Outline each uninfected red blood cell.
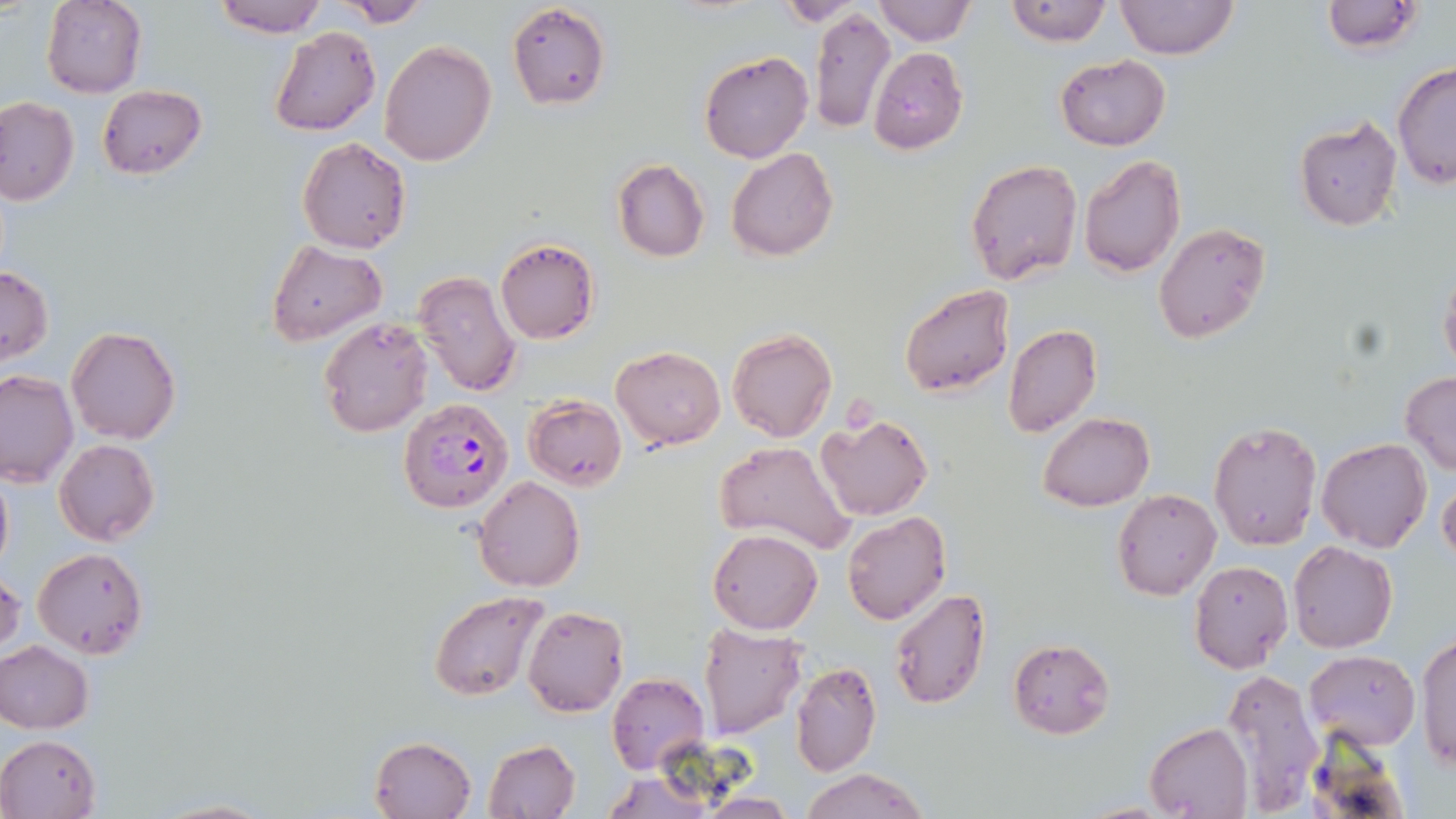

Approximate bounding boxes as (x1,y1)-(x2,y2) corner pairs in pixels.
Uninfected red blood cells: (41,0)-(147,98), (211,0)-(327,38), (337,0)-(432,27), (872,0)-(975,46), (1005,0)-(1111,46), (1113,0)-(1238,61), (776,1)-(862,24), (1321,1)-(1422,53), (506,2)-(611,112), (810,8)-(896,134), (269,27)-(380,136), (378,40)-(497,166), (869,47)-(969,151), (699,50)-(813,163), (1055,55)-(1170,151), (1392,61)-(1456,191), (97,84)-(206,179), (0,96)-(79,206), (1294,117)-(1402,231), (298,137)-(412,255), (725,147)-(839,261), (1079,154)-(1185,277), (612,159)-(709,263), (965,159)-(1083,285), (1153,221)-(1271,345), (494,237)-(600,345), (264,240)-(386,346), (1438,263)-(1456,376), (0,264)-(53,366), (413,270)-(520,397), (899,285)-(1015,398), (318,317)-(433,437), (1003,323)-(1101,436), (66,325)-(181,444), (726,327)-(837,443), (612,345)-(725,450), (0,369)-(78,488), (1401,372)-(1456,474), (523,395)-(627,490), (1039,411)-(1154,511), (815,414)-(933,521), (1208,420)-(1323,551), (1317,438)-(1432,553), (54,439)-(159,546), (715,440)-(857,556), (0,465)-(13,574), (473,475)-(585,593), (1439,482)-(1456,569), (1113,488)-(1220,601), (841,513)-(951,625), (708,530)-(822,634), (1288,541)-(1397,653), (32,547)-(149,659), (1189,559)-(1294,674), (0,571)-(23,660), (889,588)-(991,710), (428,590)-(549,702), (522,605)-(629,717), (698,623)-(809,737), (1416,633)-(1456,771), (1006,637)-(1116,740), (0,641)-(94,733), (1306,650)-(1420,750), (791,662)-(881,776), (1219,667)-(1325,813), (606,673)-(709,775), (1144,723)-(1252,819), (0,734)-(101,818), (369,735)-(475,818), (482,739)-(580,819), (802,769)-(926,819), (699,794)-(801,817), (152,798)-(273,819).

Plasmodium falciparum-infected red blood cell locations: (398,398)-(513,514). Slide-level diagnosis: Plasmodium falciparum. Thin blood smear. Captured at 1000x magnification. Image is 1456×819 pixels. May-Grünwald-Giemsa-stained preparation. Single field of view. Light microscopy.